Describe the morphology of the erythrocytes.
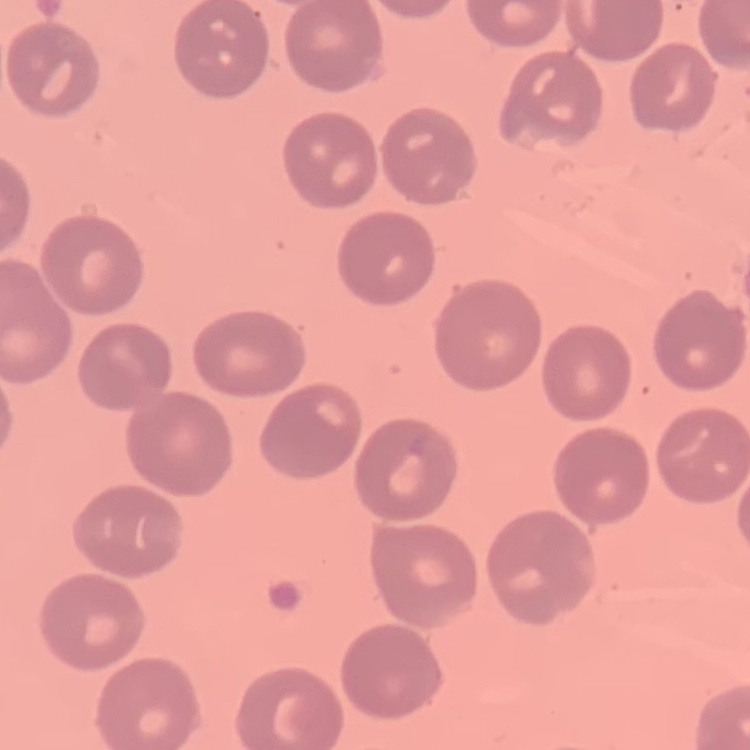
No rouleaux formation.

stain = Field's or Giemsa
preparation = thin blood film
image type = one tile cut from a larger photomicrograph